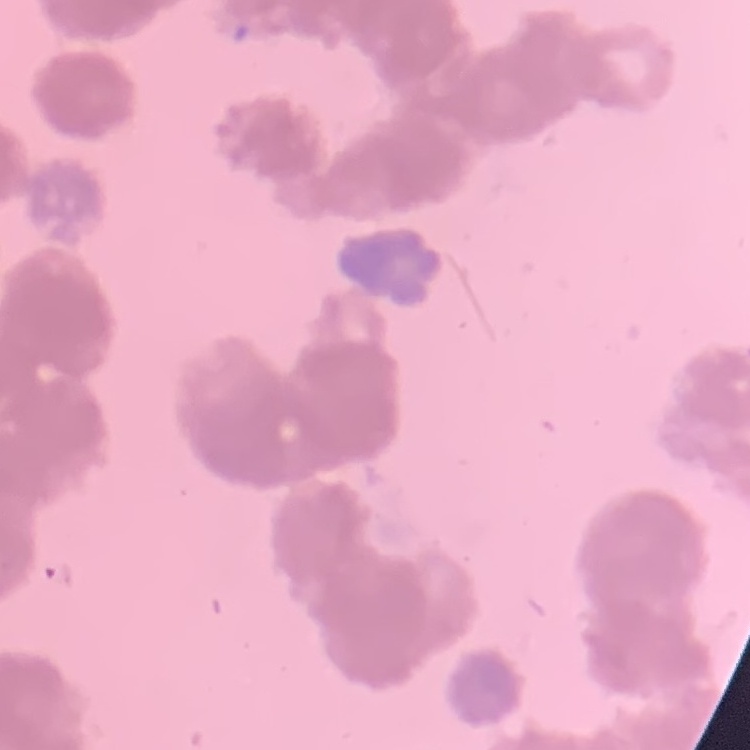

Summary:
  - Red blood cell morphology: rouleaux formation
  - Stain: Field's or Giemsa
  - Image type: square crop of a larger photomicrograph
  - Preparation: thin peripheral smear